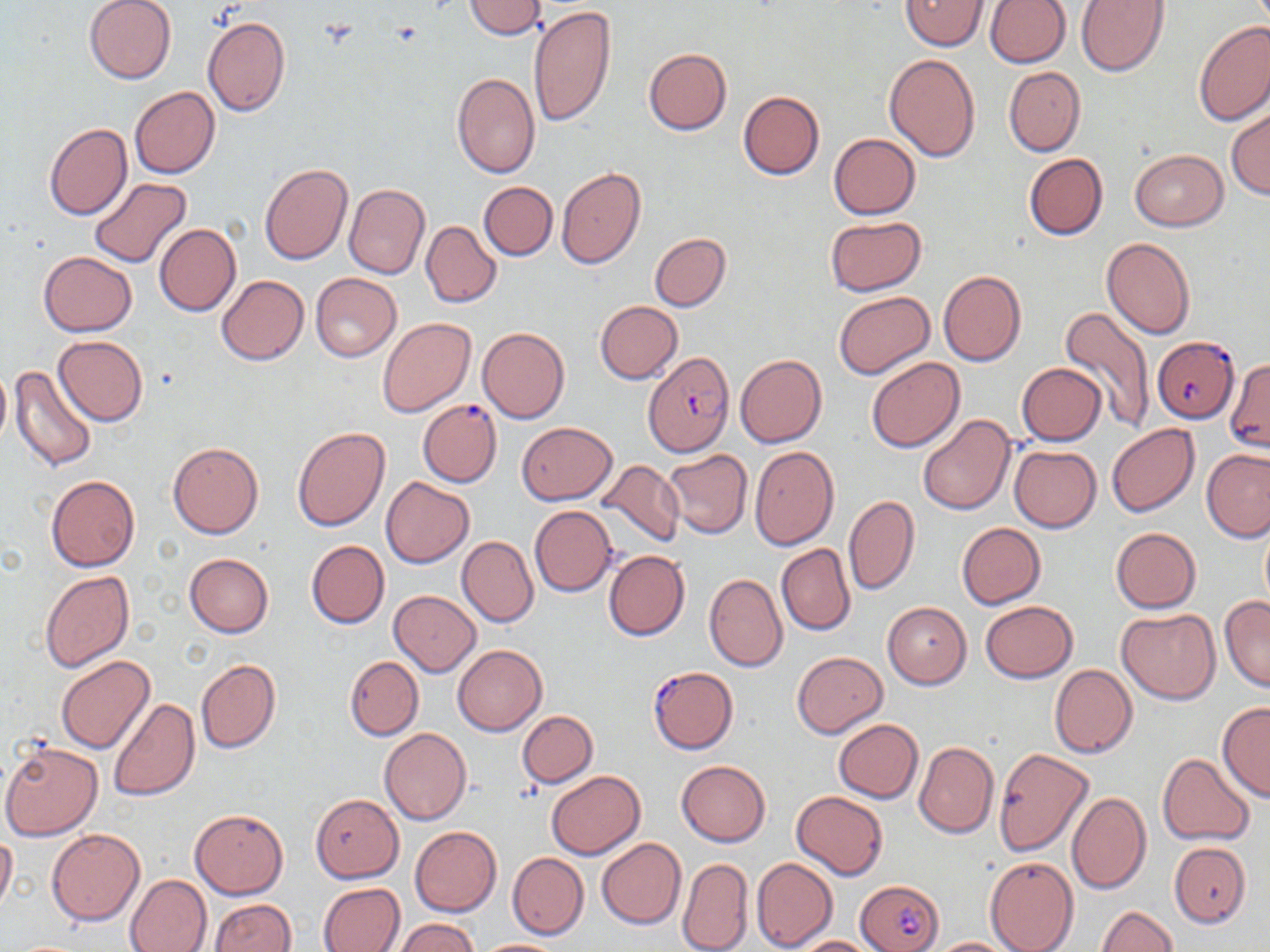
slide_level_diagnosis: Plasmodium falciparum
uninfected_red_blood_cell_locations_subset: 'approximate bounding boxes as named x1/y1/x2/y2 corners in pixels: (x1=84, y1=0, x2=176, y2=84), (x1=464, y1=0, x2=548, y2=39), (x1=900, y1=0, x2=988, y2=51), (x1=986, y1=0, x2=1070, y2=67), (x1=1075, y1=0, x2=1170, y2=76), (x1=528, y1=5, x2=615, y2=129), (x1=202, y1=16, x2=291, y2=118), (x1=1194, y1=21, x2=1270, y2=126), (x1=643, y1=48, x2=731, y2=135), (x1=883, y1=54, x2=980, y2=161), (x1=1003, y1=67, x2=1085, y2=155), (x1=452, y1=73, x2=540, y2=178), (x1=130, y1=87, x2=220, y2=178), (x1=738, y1=90, x2=825, y2=180), (x1=1226, y1=108, x2=1270, y2=199), (x1=43, y1=123, x2=131, y2=220), (x1=828, y1=133, x2=920, y2=219), (x1=1131, y1=149, x2=1227, y2=231), (x1=1023, y1=153, x2=1108, y2=240), (x1=259, y1=163, x2=353, y2=264), (x1=556, y1=167, x2=645, y2=269), (x1=88, y1=177, x2=192, y2=268), (x1=479, y1=182, x2=557, y2=260), (x1=344, y1=183, x2=429, y2=280), (x1=825, y1=216, x2=927, y2=295), (x1=421, y1=221, x2=500, y2=308), (x1=154, y1=223, x2=240, y2=316), (x1=650, y1=233, x2=731, y2=311), (x1=1101, y1=237, x2=1195, y2=341), (x1=38, y1=250, x2=137, y2=336), (x1=939, y1=271, x2=1026, y2=367), (x1=310, y1=273, x2=401, y2=362), (x1=216, y1=275, x2=309, y2=365), (x1=833, y1=292, x2=935, y2=379), (x1=595, y1=301, x2=682, y2=384), (x1=1059, y1=305, x2=1158, y2=428), (x1=378, y1=318, x2=476, y2=417), (x1=477, y1=327, x2=570, y2=423), (x1=53, y1=335, x2=148, y2=426), (x1=735, y1=354, x2=827, y2=448), (x1=866, y1=357, x2=964, y2=453), (x1=0, y1=361, x2=10, y2=452), (x1=1016, y1=363, x2=1106, y2=446), (x1=10, y1=364, x2=98, y2=473), (x1=918, y1=414, x2=1014, y2=515), (x1=517, y1=422, x2=616, y2=504), (x1=1106, y1=424, x2=1199, y2=516), (x1=293, y1=427, x2=390, y2=532), (x1=168, y1=441, x2=264, y2=539), (x1=750, y1=445, x2=839, y2=549), (x1=1009, y1=445, x2=1101, y2=532), (x1=1201, y1=449, x2=1270, y2=542), (x1=662, y1=450, x2=753, y2=539), (x1=598, y1=460, x2=685, y2=549), (x1=46, y1=475, x2=140, y2=572), (x1=381, y1=476, x2=474, y2=568), (x1=844, y1=494, x2=920, y2=595), (x1=530, y1=505, x2=618, y2=597), (x1=1259, y1=515, x2=1270, y2=613), (x1=956, y1=522, x2=1047, y2=610), (x1=1111, y1=528, x2=1201, y2=612), (x1=457, y1=536, x2=538, y2=627), (x1=306, y1=540, x2=389, y2=628), (x1=776, y1=544, x2=855, y2=636), (x1=604, y1=549, x2=689, y2=641), (x1=183, y1=554, x2=274, y2=637), (x1=40, y1=571, x2=134, y2=673), (x1=704, y1=572, x2=787, y2=672), (x1=389, y1=591, x2=481, y2=675), (x1=1219, y1=596, x2=1270, y2=694), (x1=980, y1=600, x2=1077, y2=683), (x1=882, y1=602, x2=971, y2=688), (x1=1116, y1=608, x2=1219, y2=705), (x1=453, y1=644, x2=547, y2=736), (x1=791, y1=651, x2=887, y2=738), (x1=56, y1=655, x2=154, y2=754), (x1=345, y1=656, x2=424, y2=740), (x1=195, y1=659, x2=281, y2=754), (x1=1049, y1=664, x2=1137, y2=758), (x1=108, y1=698, x2=200, y2=801), (x1=1217, y1=702, x2=1270, y2=801), (x1=518, y1=710, x2=597, y2=786), (x1=833, y1=718, x2=923, y2=803), (x1=379, y1=728, x2=471, y2=825), (x1=1, y1=742, x2=103, y2=841), (x1=914, y1=742, x2=999, y2=838), (x1=993, y1=749, x2=1094, y2=856), (x1=1158, y1=753, x2=1255, y2=845), (x1=676, y1=760, x2=771, y2=847), (x1=547, y1=770, x2=645, y2=860), (x1=791, y1=791, x2=887, y2=880), (x1=1067, y1=792, x2=1151, y2=894), (x1=310, y1=794, x2=403, y2=882), (x1=190, y1=808, x2=288, y2=898), (x1=410, y1=826, x2=501, y2=916), (x1=46, y1=828, x2=144, y2=925), (x1=0, y1=830, x2=16, y2=917), (x1=596, y1=838, x2=686, y2=929), (x1=507, y1=852, x2=588, y2=938), (x1=985, y1=856, x2=1079, y2=952), (x1=678, y1=858, x2=752, y2=952), (x1=750, y1=858, x2=838, y2=951), (x1=125, y1=874, x2=212, y2=952), (x1=317, y1=882, x2=404, y2=952), (x1=207, y1=899, x2=296, y2=952), (x1=1096, y1=906, x2=1178, y2=952), (x1=396, y1=918, x2=481, y2=952), (x1=791, y1=935, x2=878, y2=952), (x1=925, y1=937, x2=1021, y2=951), (x1=474, y1=939, x2=568, y2=952)'
modality: light microscopy
plasmodium_falciparum_infected_red_blood_cell_locations_subset: 'approximate bounding boxes as named x1/y1/x2/y2 corners in pixels: (x1=1153, y1=337, x2=1240, y2=422), (x1=646, y1=352, x2=734, y2=458), (x1=418, y1=400, x2=501, y2=487), (x1=647, y1=666, x2=739, y2=754), (x1=858, y1=879, x2=945, y2=952)'
preparation: thin blood film
stain: May-Grünwald-Giemsa
magnification: 1000x
field_of_view: single
image_size: 1270×952 pixels